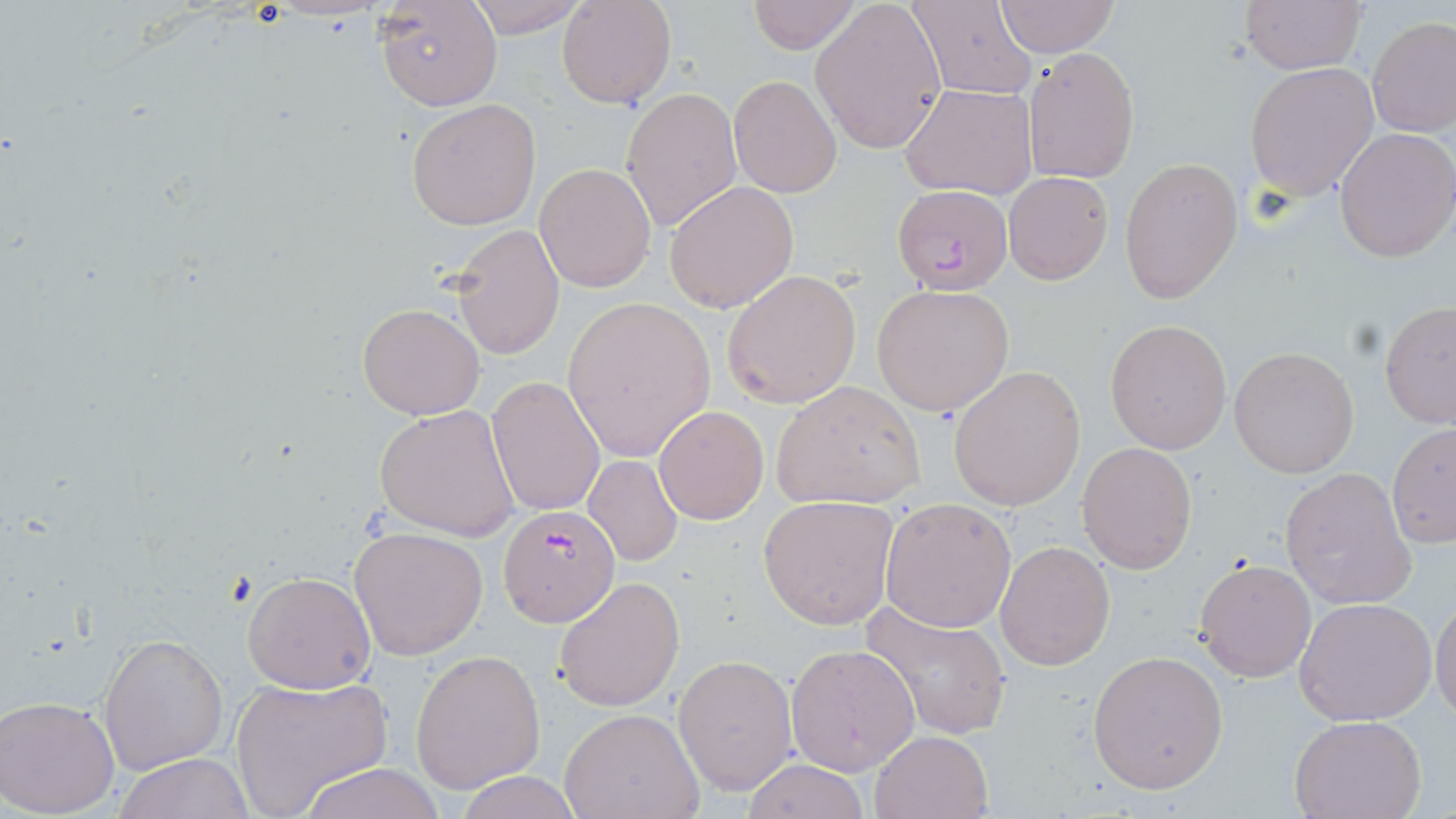

Approximate bounding boxes as (x1,y1)-(x2,y2) corner pairs in pixels. Uninfected red blood cell locations: (464,0)-(592,38), (557,0)-(675,109), (747,0)-(860,53), (910,0)-(1038,99), (1239,0)-(1366,75), (372,1)-(502,111), (996,1)-(1119,56), (809,2)-(947,154), (1367,17)-(1456,138), (1022,47)-(1140,185), (1245,62)-(1379,200), (728,74)-(842,198), (901,83)-(1039,200), (620,87)-(742,232), (407,98)-(543,231), (1333,127)-(1456,263), (1120,157)-(1243,302), (532,162)-(656,293), (1003,173)-(1113,284), (664,181)-(799,312), (449,220)-(564,361), (721,270)-(863,410), (871,284)-(1015,417), (561,295)-(716,463), (1380,301)-(1456,429), (357,302)-(484,420), (1106,320)-(1233,454), (1230,346)-(1359,477), (948,364)-(1087,511), (486,376)-(606,516), (771,380)-(925,510), (374,402)-(521,541), (653,404)-(769,526), (1387,422)-(1456,547), (1077,441)-(1197,573), (584,454)-(683,567), (1280,468)-(1417,609), (758,496)-(897,629), (880,496)-(1019,633), (350,526)-(487,659), (994,538)-(1115,671), (1194,558)-(1316,683), (243,571)-(376,693), (554,575)-(686,712), (1430,591)-(1456,725), (1293,597)-(1437,726), (859,599)-(1014,739), (99,633)-(228,773), (786,643)-(919,775), (411,649)-(546,793), (1087,651)-(1228,794), (673,654)-(796,793), (227,676)-(392,818), (0,694)-(122,816), (560,707)-(704,819), (1288,715)-(1425,819), (869,729)-(993,818), (112,752)-(255,819), (740,759)-(871,818), (292,762)-(452,819), (457,772)-(584,818). Plasmodium falciparum-infected red blood cell locations: (893,184)-(1013,296), (498,503)-(620,627). Slide-level diagnosis: Plasmodium falciparum. Optical microscopy. May-Grünwald-Giemsa stain. Thin blood smear. Single field of view. Captured at 1000x magnification. Image is 1456×819 pixels.